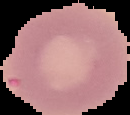
image type = segmented cell region with the area outside set to black
malaria status = uninfected
preparation = thin blood smear
image size = 130×115 pixels